Point out each Plasmodium parasite.
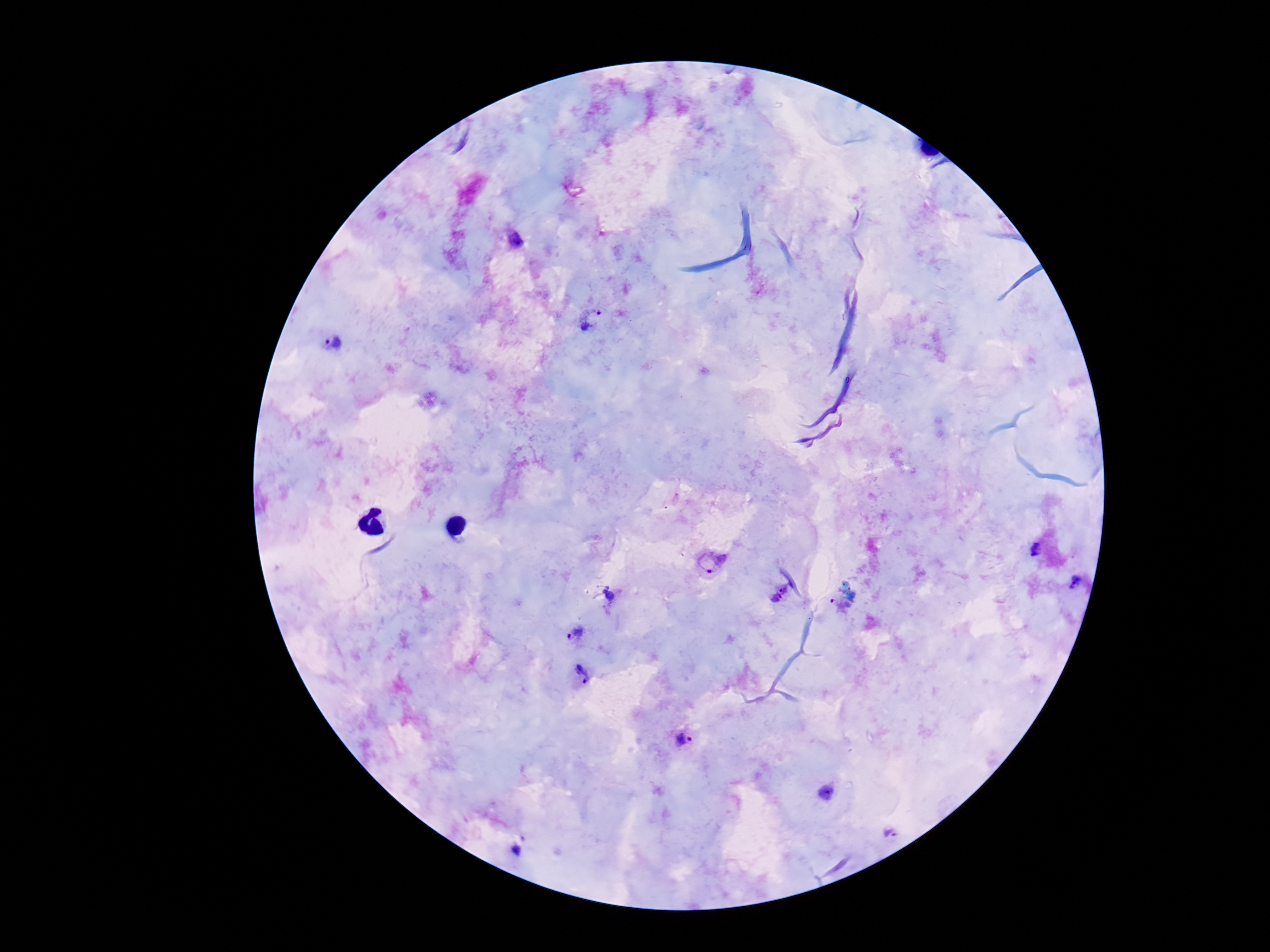

Approximate centers as (x, y) in pixels.
Plasmodium parasites: (592, 321), (334, 342), (1035, 549), (710, 565), (1074, 582), (779, 592), (842, 604), (573, 633), (581, 676), (683, 740), (890, 833).

Summary:
  - Magnification: 100x
  - Field of view: single
  - Preparation: thick blood smear
  - Capture: smartphone camera through the microscope eyepiece
  - Image size: 1270×952 pixels
  - Patient malaria status: positive
  - Stain: Giemsa